Assess this cell for malaria.
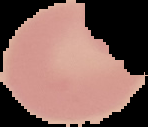
It is uninfected.

image size = 148×127 pixels
image type = cell region segmented out of the field of view; surrounding area masked to black
preparation = thin blood film